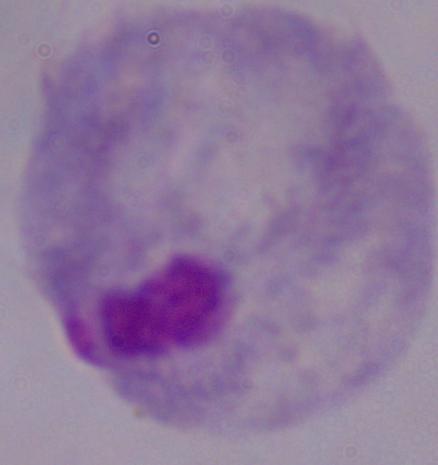
Summary:
  - Magnification: 1000x
  - Identification: trichomonad
  - Modality: micrograph